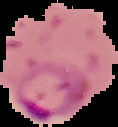
Summary:
  - Image size: 118×127 pixels
  - Preparation: thin blood smear
  - Image type: segmented cell region on a black background
  - Result: malaria parasites detected